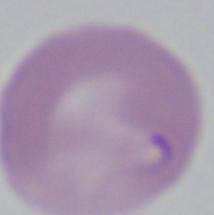

Micrograph. A Babesia parasite is seen. Captured at 1000x magnification.